Comment on the background quality.
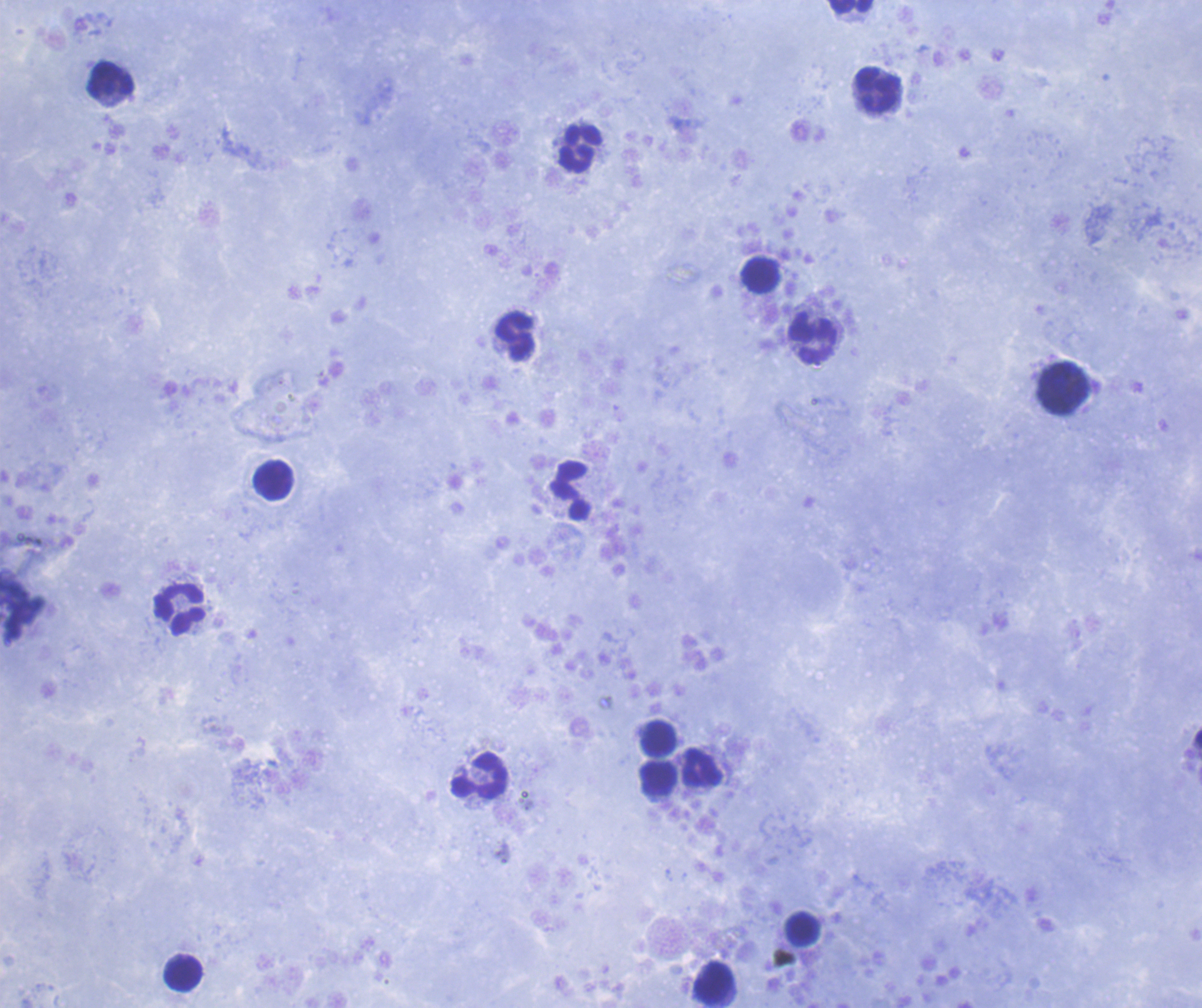
It is good.

coordinate format = approximate centers as (x, y) in pixels
leukocyte locations = (850, 6), (111, 81), (877, 90), (579, 149), (760, 275), (515, 336), (812, 340), (1062, 387), (273, 481), (571, 491), (180, 610), (658, 739), (703, 769), (479, 776), (659, 779), (803, 929), (183, 972), (715, 982)
context = previously used in an actual diagnosis
magnification = 100x
image size = 1202×1008 pixels
field of view = single
stain = Romanowsky
coloration quality = good
preparation = thick blood film
result = no malaria parasites detected